Locate and identify every blood parasite.
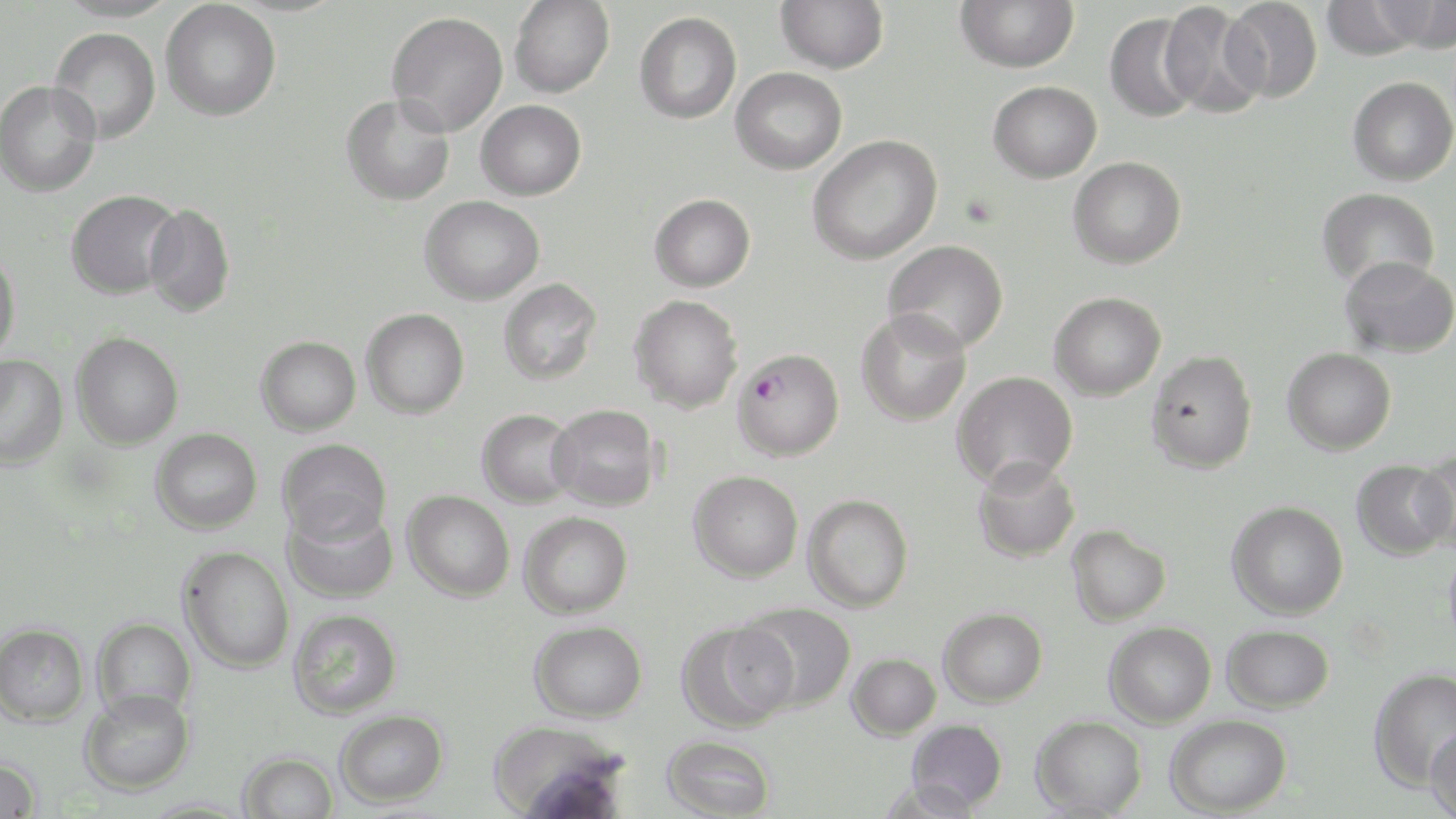

Approximate bounding boxes as named x1/y1/x2/y2 corners in pixels.
Plasmodium falciparum-infected red blood cells: (x1=733, y1=347, x2=844, y2=460).
No Plasmodium ovale, Plasmodium malariae, Plasmodium vivax, Babesia divergens, or Trypanosoma brucei observed.

{
  "slide_level_diagnosis": "Plasmodium falciparum",
  "magnification": "1000x",
  "modality": "optical microscopy",
  "field_of_view": "one of a larger specimen",
  "image_size": "1456×819 pixels",
  "stain": "May-Grünwald-Giemsa",
  "preparation": "thin blood smear",
  "uninfected_red_blood_cell_locations": "approximate bounding boxes as named x1/y1/x2/y2 corners in pixels: (x1=161, y1=0, x2=282, y2=121), (x1=509, y1=0, x2=614, y2=98), (x1=776, y1=0, x2=889, y2=74), (x1=955, y1=0, x2=1079, y2=73), (x1=1222, y1=0, x2=1323, y2=103), (x1=1372, y1=0, x2=1455, y2=52), (x1=1320, y1=1, x2=1425, y2=60), (x1=1161, y1=2, x2=1267, y2=117), (x1=387, y1=11, x2=508, y2=136), (x1=634, y1=11, x2=742, y2=124), (x1=1104, y1=12, x2=1202, y2=122), (x1=49, y1=28, x2=161, y2=143), (x1=730, y1=67, x2=847, y2=175), (x1=1347, y1=76, x2=1456, y2=186), (x1=0, y1=79, x2=102, y2=197), (x1=988, y1=81, x2=1102, y2=183), (x1=341, y1=93, x2=455, y2=206), (x1=475, y1=99, x2=586, y2=200), (x1=807, y1=134, x2=942, y2=265), (x1=1068, y1=156, x2=1187, y2=269), (x1=1316, y1=186, x2=1440, y2=290), (x1=65, y1=189, x2=182, y2=299), (x1=649, y1=193, x2=756, y2=292), (x1=420, y1=195, x2=545, y2=305), (x1=143, y1=204, x2=236, y2=317), (x1=883, y1=239, x2=1009, y2=353), (x1=0, y1=249, x2=20, y2=361), (x1=1340, y1=255, x2=1456, y2=359), (x1=498, y1=278, x2=602, y2=385), (x1=1049, y1=291, x2=1166, y2=400), (x1=628, y1=295, x2=744, y2=413), (x1=361, y1=308, x2=469, y2=418), (x1=857, y1=309, x2=972, y2=425), (x1=71, y1=332, x2=183, y2=449), (x1=255, y1=336, x2=361, y2=436), (x1=1282, y1=347, x2=1396, y2=455), (x1=1146, y1=349, x2=1258, y2=474), (x1=0, y1=355, x2=68, y2=469), (x1=952, y1=371, x2=1078, y2=490), (x1=547, y1=403, x2=661, y2=510), (x1=477, y1=408, x2=579, y2=507), (x1=150, y1=427, x2=262, y2=534), (x1=278, y1=438, x2=392, y2=544), (x1=1415, y1=452, x2=1456, y2=557), (x1=972, y1=457, x2=1081, y2=563), (x1=1351, y1=459, x2=1454, y2=561), (x1=688, y1=470, x2=803, y2=582), (x1=403, y1=490, x2=514, y2=602), (x1=803, y1=494, x2=913, y2=612), (x1=1226, y1=501, x2=1348, y2=619), (x1=283, y1=503, x2=398, y2=604), (x1=519, y1=511, x2=632, y2=619), (x1=1066, y1=524, x2=1171, y2=626), (x1=1443, y1=543, x2=1456, y2=657), (x1=178, y1=546, x2=294, y2=673), (x1=738, y1=602, x2=857, y2=712), (x1=938, y1=607, x2=1048, y2=707), (x1=288, y1=609, x2=402, y2=719), (x1=92, y1=617, x2=196, y2=720), (x1=530, y1=620, x2=647, y2=723), (x1=675, y1=620, x2=795, y2=732), (x1=1104, y1=621, x2=1216, y2=728), (x1=0, y1=622, x2=89, y2=726), (x1=1222, y1=624, x2=1334, y2=713), (x1=846, y1=653, x2=941, y2=740), (x1=1368, y1=667, x2=1456, y2=792), (x1=80, y1=689, x2=195, y2=795), (x1=335, y1=709, x2=448, y2=808), (x1=1165, y1=713, x2=1292, y2=817), (x1=1031, y1=714, x2=1148, y2=817), (x1=487, y1=719, x2=628, y2=817), (x1=906, y1=719, x2=1008, y2=812), (x1=1424, y1=725, x2=1456, y2=819), (x1=661, y1=734, x2=776, y2=819), (x1=239, y1=751, x2=339, y2=818), (x1=0, y1=755, x2=42, y2=818), (x1=877, y1=778, x2=981, y2=819)"
}